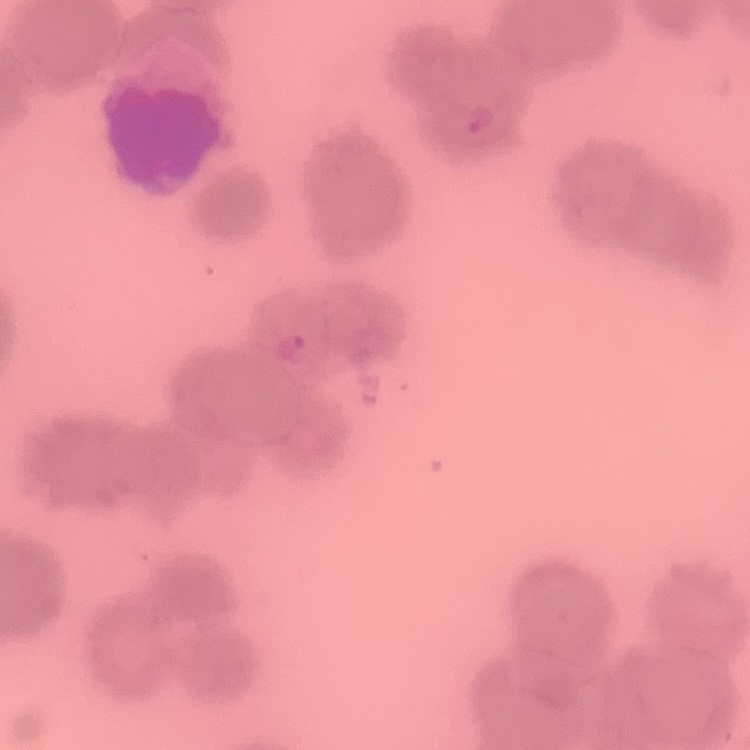

Summary:
  - Erythrocyte morphology: rouleaux formation
  - Image type: one tile cut from a larger photomicrograph
  - Stain: Field's or Giemsa
  - Preparation: thin peripheral smear